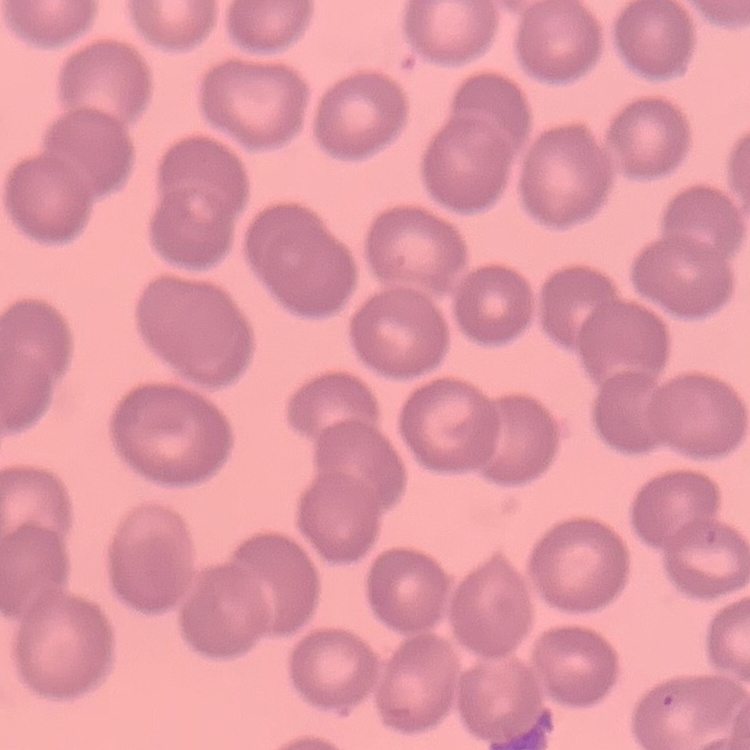
Summary:
  - Erythrocyte morphology: no rouleaux formation
  - Stain: Field's or Giemsa
  - Preparation: thin blood smear
  - Image type: one tile cut from a larger photomicrograph